Describe the morphology of the red blood cells.
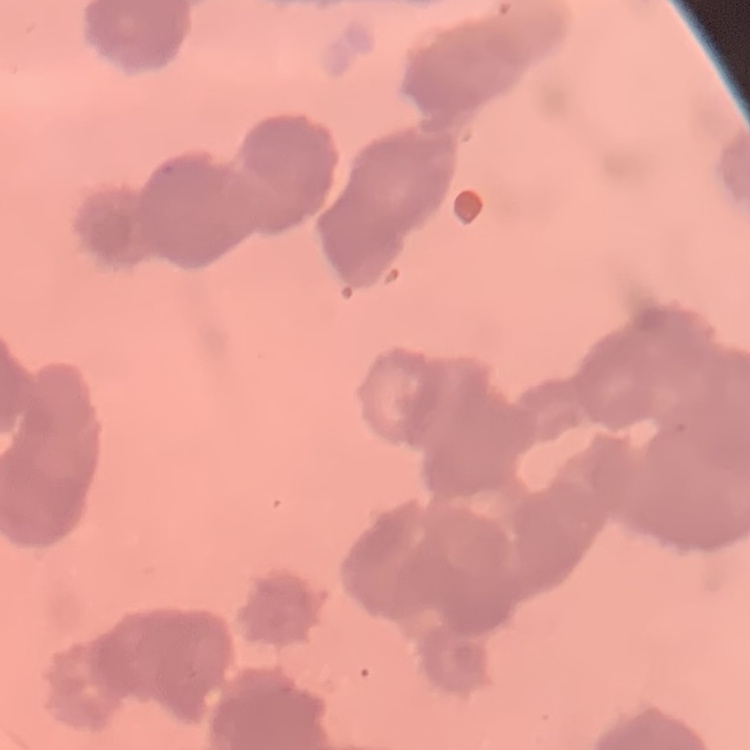
Rouleaux formation.

Field's or Giemsa stain. Thin blood smear. One tile cut from a larger photomicrograph.